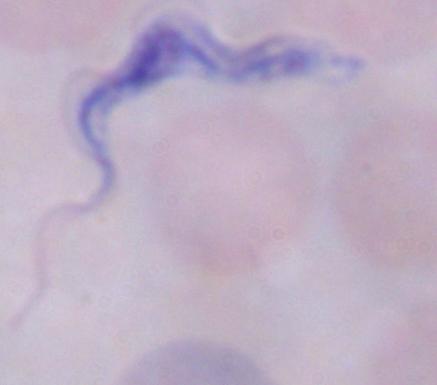

modality = micrograph
identification = trypanosome
magnification = 1000x